Classify this cell by malaria status.
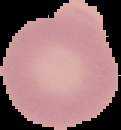
It is uninfected.

From a thin blood film. Image is 121×130 pixels. Segmented cell region on a black background.